Name the parasite shown.
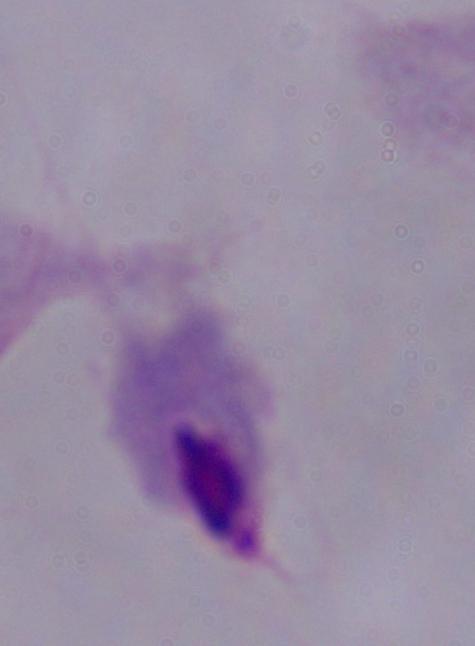
This is a trichomonad.

magnification = 1000x
modality = micrograph